Identify the cell.
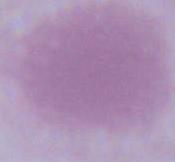
This is an erythrocyte.

Photomicrograph. 1000x magnification.